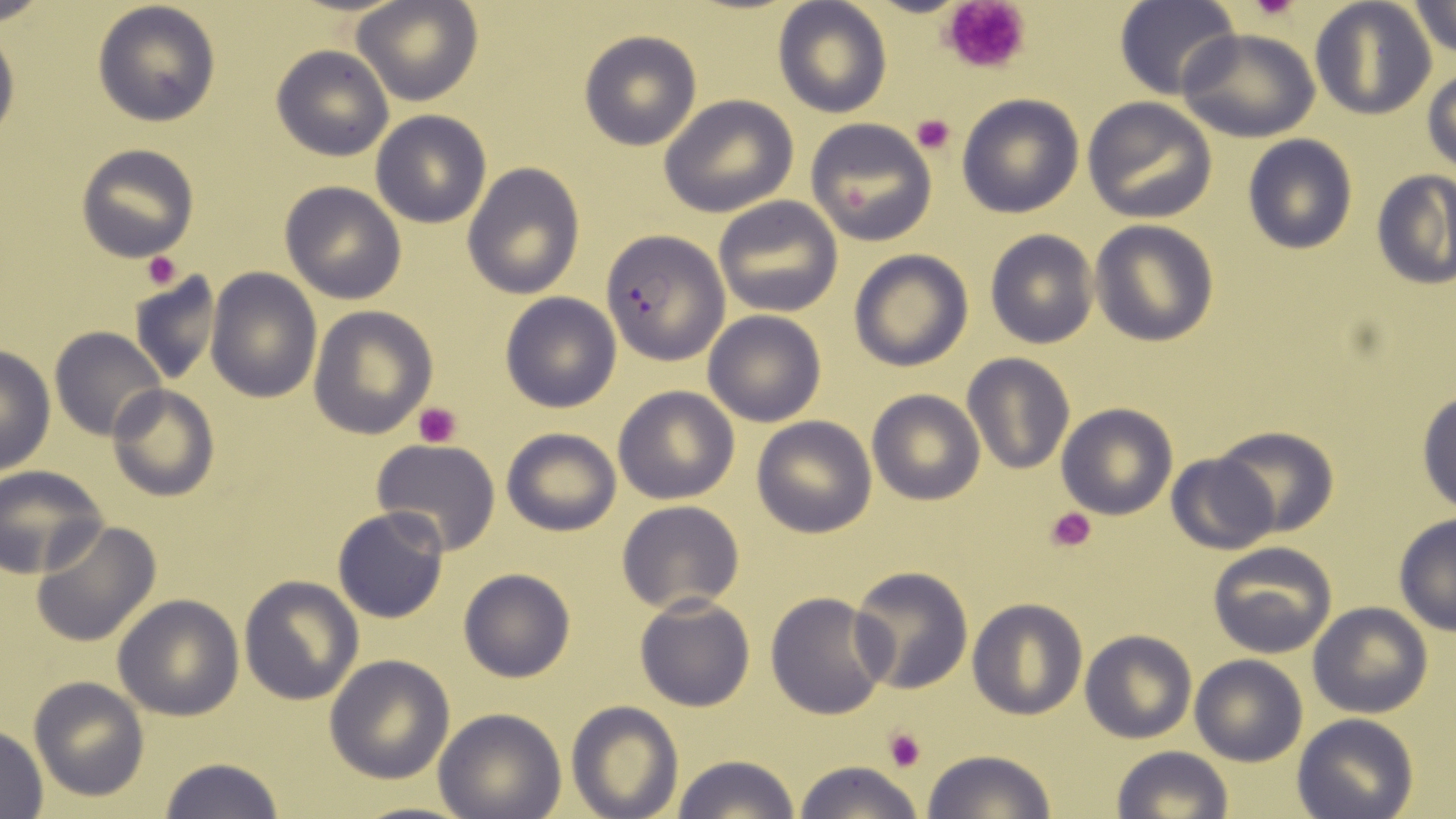 Approximate bounding boxes as named x1/y1/x2/y2 corners in pixels. Plasmodium falciparum-infected red blood cell locations: (x1=600, y1=231, x2=729, y2=363). Platelet locations: (x1=941, y1=0, x2=1033, y2=75), (x1=1249, y1=0, x2=1302, y2=23), (x1=909, y1=113, x2=955, y2=156), (x1=140, y1=251, x2=184, y2=290), (x1=413, y1=401, x2=461, y2=449), (x1=1044, y1=507, x2=1096, y2=553), (x1=884, y1=726, x2=927, y2=770). Uninfected red blood cell locations: (x1=92, y1=0, x2=221, y2=126), (x1=1309, y1=0, x2=1437, y2=119), (x1=1407, y1=0, x2=1456, y2=60), (x1=353, y1=1, x2=482, y2=106), (x1=1114, y1=1, x2=1239, y2=99), (x1=773, y1=2, x2=892, y2=118), (x1=0, y1=23, x2=19, y2=148), (x1=1179, y1=27, x2=1318, y2=141), (x1=579, y1=29, x2=702, y2=150), (x1=271, y1=46, x2=394, y2=162), (x1=1423, y1=68, x2=1456, y2=173), (x1=957, y1=93, x2=1084, y2=217), (x1=659, y1=94, x2=799, y2=216), (x1=1083, y1=97, x2=1218, y2=224), (x1=371, y1=110, x2=491, y2=227), (x1=804, y1=118, x2=940, y2=246), (x1=1242, y1=135, x2=1357, y2=254), (x1=75, y1=143, x2=200, y2=263), (x1=463, y1=163, x2=585, y2=298), (x1=1372, y1=171, x2=1455, y2=291), (x1=280, y1=181, x2=406, y2=304), (x1=713, y1=196, x2=843, y2=317), (x1=1089, y1=220, x2=1219, y2=347), (x1=985, y1=229, x2=1099, y2=349), (x1=848, y1=250, x2=974, y2=371), (x1=206, y1=268, x2=322, y2=402), (x1=131, y1=270, x2=226, y2=388), (x1=500, y1=291, x2=621, y2=413), (x1=307, y1=303, x2=437, y2=439), (x1=702, y1=310, x2=826, y2=427), (x1=50, y1=327, x2=166, y2=442), (x1=0, y1=344, x2=56, y2=476), (x1=962, y1=353, x2=1074, y2=476), (x1=107, y1=385, x2=218, y2=501), (x1=613, y1=385, x2=739, y2=504), (x1=867, y1=389, x2=984, y2=504), (x1=1415, y1=390, x2=1456, y2=515), (x1=1055, y1=403, x2=1177, y2=519), (x1=751, y1=417, x2=876, y2=537), (x1=1214, y1=426, x2=1337, y2=539), (x1=501, y1=428, x2=621, y2=535), (x1=370, y1=438, x2=501, y2=557), (x1=1166, y1=453, x2=1279, y2=555), (x1=1, y1=466, x2=108, y2=578), (x1=615, y1=500, x2=746, y2=614), (x1=332, y1=506, x2=449, y2=624), (x1=1393, y1=515, x2=1456, y2=634), (x1=31, y1=518, x2=161, y2=649), (x1=1207, y1=542, x2=1336, y2=657), (x1=850, y1=566, x2=973, y2=695), (x1=458, y1=568, x2=576, y2=684), (x1=239, y1=575, x2=363, y2=704), (x1=764, y1=592, x2=893, y2=720), (x1=112, y1=595, x2=244, y2=720), (x1=635, y1=595, x2=756, y2=711), (x1=968, y1=600, x2=1086, y2=719), (x1=1307, y1=602, x2=1433, y2=718), (x1=1080, y1=630, x2=1196, y2=743), (x1=325, y1=654, x2=455, y2=784), (x1=1189, y1=654, x2=1307, y2=766), (x1=28, y1=676, x2=150, y2=802), (x1=567, y1=701, x2=680, y2=818), (x1=434, y1=709, x2=567, y2=818), (x1=1293, y1=714, x2=1419, y2=819), (x1=0, y1=726, x2=50, y2=817), (x1=1111, y1=746, x2=1233, y2=819), (x1=921, y1=749, x2=1058, y2=819), (x1=668, y1=755, x2=804, y2=818), (x1=158, y1=756, x2=286, y2=819), (x1=790, y1=760, x2=926, y2=819). Slide-level diagnosis: Plasmodium falciparum. Captured at 1000x magnification. Optical microscopy. Thin blood smear. One field of a larger specimen. May-Grünwald-Giemsa stain. Image is 1456×819 pixels.